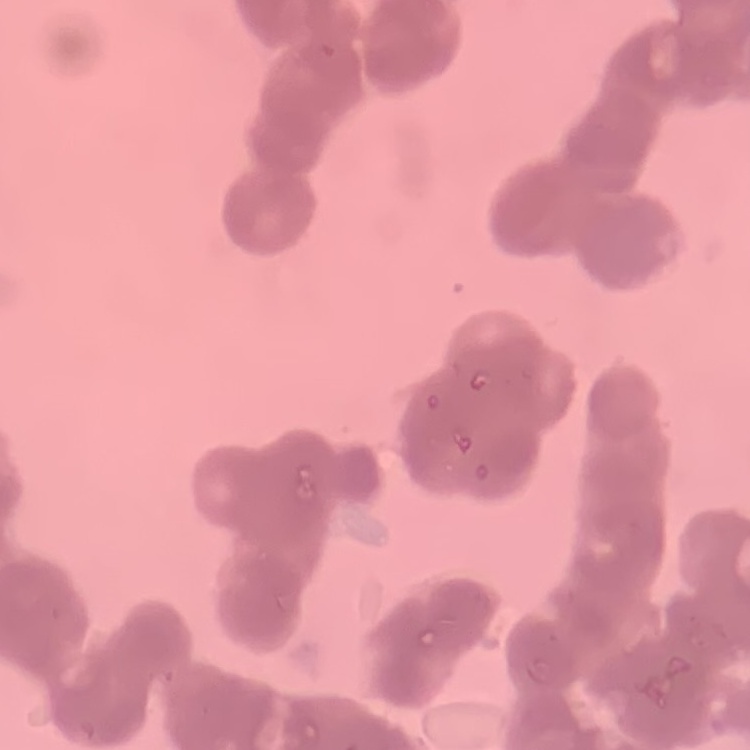

Summary:
  - Erythrocyte morphology: rouleaux formation
  - Stain: Field's or Giemsa
  - Preparation: thin blood smear
  - Image type: one tile cut from a larger photomicrograph